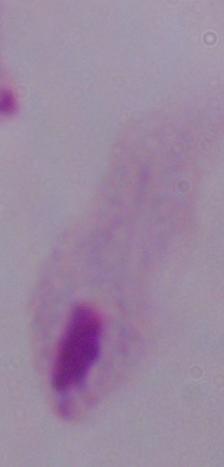

magnification = 1000x
modality = micrograph
identification = trichomonad